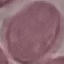
Result: negative for malaria parasites. Automatically extracted cell patch, resized to 64 × 64 pixels. Giemsa stain. Acquired by smartphone through the microscope eyepiece. Thin blood smear.